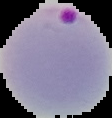

Summary:
  - Result: Plasmodium parasites detected
  - Image size: 112×118 pixels
  - Preparation: thin blood film
  - Image type: segmented cell region with the area outside set to black